Assess the morphology of the red blood cells.
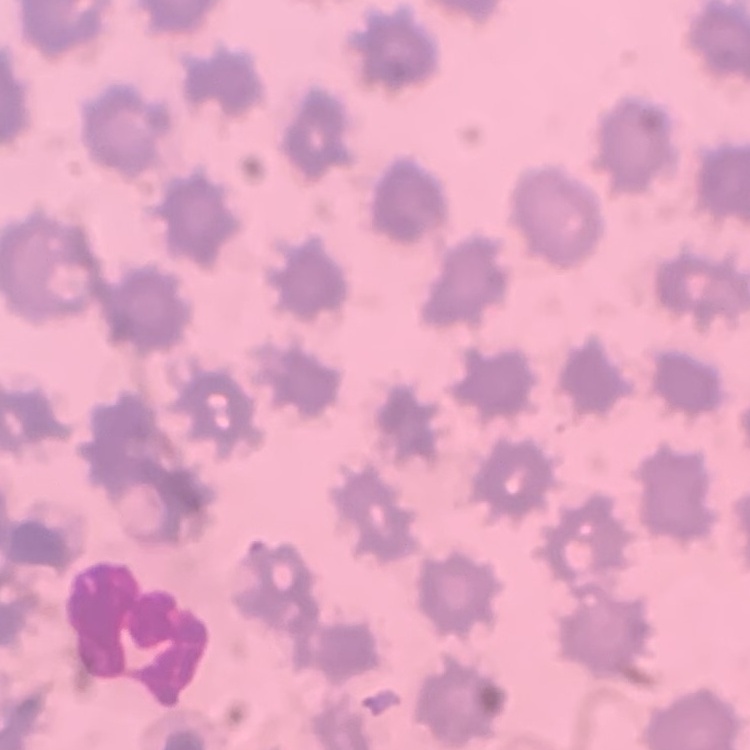

No rouleaux formation.

Summary:
  - Image type: square crop of a larger photomicrograph
  - Preparation: thin blood film
  - Stain: Field's or Giemsa